State which cell type is depicted.
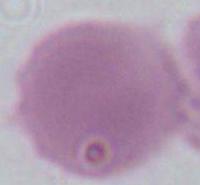

This is an erythrocyte.

Summary:
  - Magnification: 1000x
  - Modality: photomicrograph